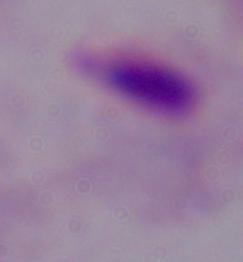
A trichomonad is shown. 1000x magnification. Photomicrograph.